Point out cells.
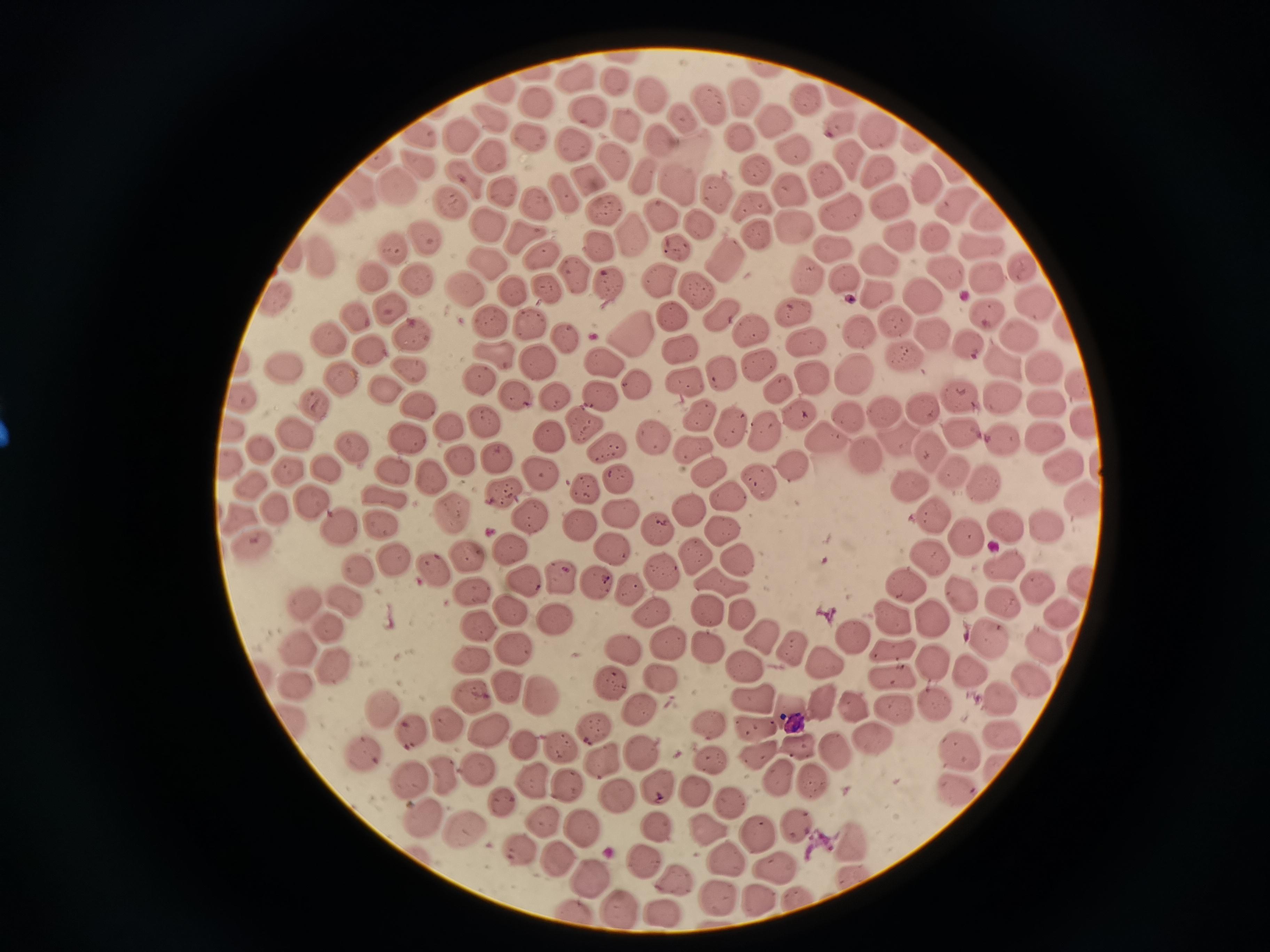
Approximate object centers, in pixels from the top-left corner.
Cells: (x=769, y=69), (x=577, y=76), (x=612, y=77), (x=654, y=91), (x=503, y=92), (x=807, y=98), (x=742, y=99), (x=708, y=102), (x=536, y=103), (x=583, y=109), (x=487, y=115), (x=627, y=122), (x=773, y=125), (x=841, y=126), (x=422, y=132), (x=881, y=132), (x=460, y=136), (x=738, y=136), (x=527, y=137), (x=658, y=137), (x=911, y=141), (x=571, y=142), (x=787, y=150), (x=491, y=154), (x=613, y=156), (x=850, y=160), (x=414, y=163), (x=873, y=165), (x=753, y=169), (x=641, y=174), (x=462, y=176), (x=818, y=179), (x=926, y=181), (x=677, y=182), (x=591, y=183), (x=398, y=186), (x=501, y=189), (x=718, y=190), (x=563, y=193), (x=789, y=193), (x=363, y=197), (x=754, y=199), (x=883, y=199), (x=451, y=201), (x=536, y=202), (x=959, y=207), (x=338, y=208), (x=604, y=211), (x=662, y=211), (x=838, y=215), (x=993, y=220), (x=790, y=225), (x=484, y=226), (x=701, y=226), (x=753, y=229), (x=522, y=231), (x=628, y=233), (x=901, y=234), (x=420, y=235), (x=937, y=238), (x=979, y=243), (x=676, y=247), (x=831, y=249), (x=602, y=251), (x=398, y=253), (x=537, y=253), (x=730, y=255), (x=877, y=259), (x=318, y=260), (x=486, y=262), (x=1024, y=267), (x=809, y=274), (x=416, y=275), (x=947, y=275), (x=574, y=276), (x=986, y=276), (x=661, y=277), (x=375, y=278), (x=850, y=280), (x=464, y=282), (x=699, y=284), (x=614, y=285), (x=544, y=286), (x=512, y=289), (x=877, y=296), (x=924, y=297), (x=278, y=299), (x=391, y=305), (x=1034, y=305), (x=797, y=307), (x=983, y=311), (x=672, y=312), (x=721, y=312), (x=353, y=315), (x=488, y=316), (x=527, y=320), (x=753, y=325), (x=894, y=325), (x=1068, y=326), (x=857, y=330), (x=413, y=333), (x=629, y=334), (x=1014, y=335), (x=328, y=336), (x=564, y=336), (x=934, y=336), (x=801, y=339), (x=679, y=343), (x=969, y=344), (x=369, y=347), (x=494, y=349), (x=902, y=354), (x=536, y=357), (x=995, y=361), (x=602, y=362), (x=758, y=364), (x=286, y=367), (x=409, y=368), (x=1042, y=368), (x=719, y=372), (x=810, y=374), (x=852, y=374), (x=338, y=375), (x=480, y=376), (x=683, y=382), (x=635, y=384), (x=1077, y=385), (x=383, y=389), (x=780, y=389), (x=510, y=394), (x=962, y=394), (x=556, y=395), (x=599, y=396), (x=417, y=397), (x=242, y=399), (x=999, y=400), (x=316, y=403), (x=1043, y=406), (x=925, y=409), (x=884, y=411), (x=847, y=414), (x=700, y=415), (x=799, y=416), (x=483, y=417), (x=583, y=422), (x=1087, y=425), (x=731, y=426), (x=233, y=428), (x=407, y=430), (x=444, y=431), (x=764, y=431), (x=961, y=431), (x=294, y=433), (x=550, y=435), (x=652, y=437), (x=891, y=437), (x=1042, y=439), (x=827, y=441), (x=1001, y=441), (x=349, y=442), (x=605, y=445), (x=692, y=448), (x=927, y=450), (x=262, y=452), (x=458, y=453), (x=866, y=453), (x=499, y=457), (x=228, y=462), (x=794, y=465), (x=330, y=466), (x=1061, y=468), (x=539, y=470), (x=709, y=471), (x=953, y=471), (x=292, y=474), (x=395, y=474), (x=613, y=475), (x=760, y=479), (x=433, y=482), (x=251, y=483), (x=584, y=484), (x=986, y=484), (x=908, y=485), (x=504, y=490), (x=731, y=495), (x=378, y=496), (x=1081, y=497), (x=312, y=507), (x=273, y=508), (x=683, y=509), (x=525, y=512), (x=623, y=512), (x=930, y=512), (x=247, y=517), (x=1043, y=522), (x=381, y=523), (x=454, y=523), (x=585, y=524), (x=1004, y=527), (x=660, y=530), (x=720, y=531), (x=341, y=533), (x=966, y=535), (x=256, y=544), (x=514, y=550), (x=612, y=550), (x=693, y=555), (x=389, y=557), (x=466, y=557), (x=930, y=558), (x=738, y=563), (x=997, y=566), (x=435, y=570), (x=663, y=570), (x=367, y=574), (x=561, y=576), (x=521, y=580), (x=597, y=581), (x=726, y=584), (x=907, y=585), (x=1034, y=585), (x=632, y=586), (x=473, y=590), (x=964, y=594), (x=1001, y=600), (x=342, y=601), (x=306, y=604), (x=1057, y=609), (x=512, y=610), (x=706, y=611), (x=650, y=612), (x=742, y=612), (x=554, y=617), (x=888, y=617), (x=928, y=618), (x=476, y=623), (x=329, y=624), (x=763, y=635), (x=989, y=636), (x=663, y=638), (x=852, y=638), (x=706, y=640), (x=517, y=646), (x=1038, y=646), (x=622, y=647), (x=794, y=648), (x=891, y=648), (x=299, y=649), (x=470, y=656), (x=823, y=661), (x=929, y=664), (x=329, y=668), (x=969, y=668), (x=744, y=670), (x=659, y=673), (x=890, y=677), (x=610, y=680), (x=1032, y=683), (x=297, y=685), (x=505, y=686), (x=537, y=693), (x=750, y=693), (x=469, y=694), (x=995, y=694), (x=820, y=701), (x=850, y=705), (x=932, y=705), (x=786, y=707), (x=381, y=710), (x=892, y=712), (x=641, y=715), (x=446, y=723), (x=595, y=723), (x=708, y=723), (x=751, y=728), (x=488, y=731), (x=414, y=732), (x=997, y=732), (x=868, y=735), (x=525, y=744), (x=560, y=744), (x=953, y=747), (x=748, y=750), (x=362, y=751), (x=833, y=753), (x=643, y=754), (x=600, y=760), (x=707, y=761), (x=446, y=773), (x=478, y=774), (x=775, y=774), (x=530, y=777), (x=412, y=778), (x=812, y=781), (x=566, y=784), (x=657, y=785), (x=692, y=786), (x=957, y=787), (x=618, y=797), (x=501, y=799), (x=725, y=803), (x=416, y=813), (x=543, y=820), (x=798, y=821), (x=582, y=824), (x=464, y=826), (x=701, y=827), (x=655, y=829), (x=753, y=835), (x=853, y=841), (x=521, y=850), (x=721, y=858), (x=554, y=859), (x=638, y=861), (x=777, y=869), (x=592, y=873), (x=851, y=874), (x=673, y=881), (x=797, y=896), (x=752, y=897), (x=616, y=905), (x=578, y=913), (x=661, y=915).

image size = 1270×952 pixels
preparation = thin smear
stain = Giemsa
field of view = single
capture = smartphone through the microscope eyepiece